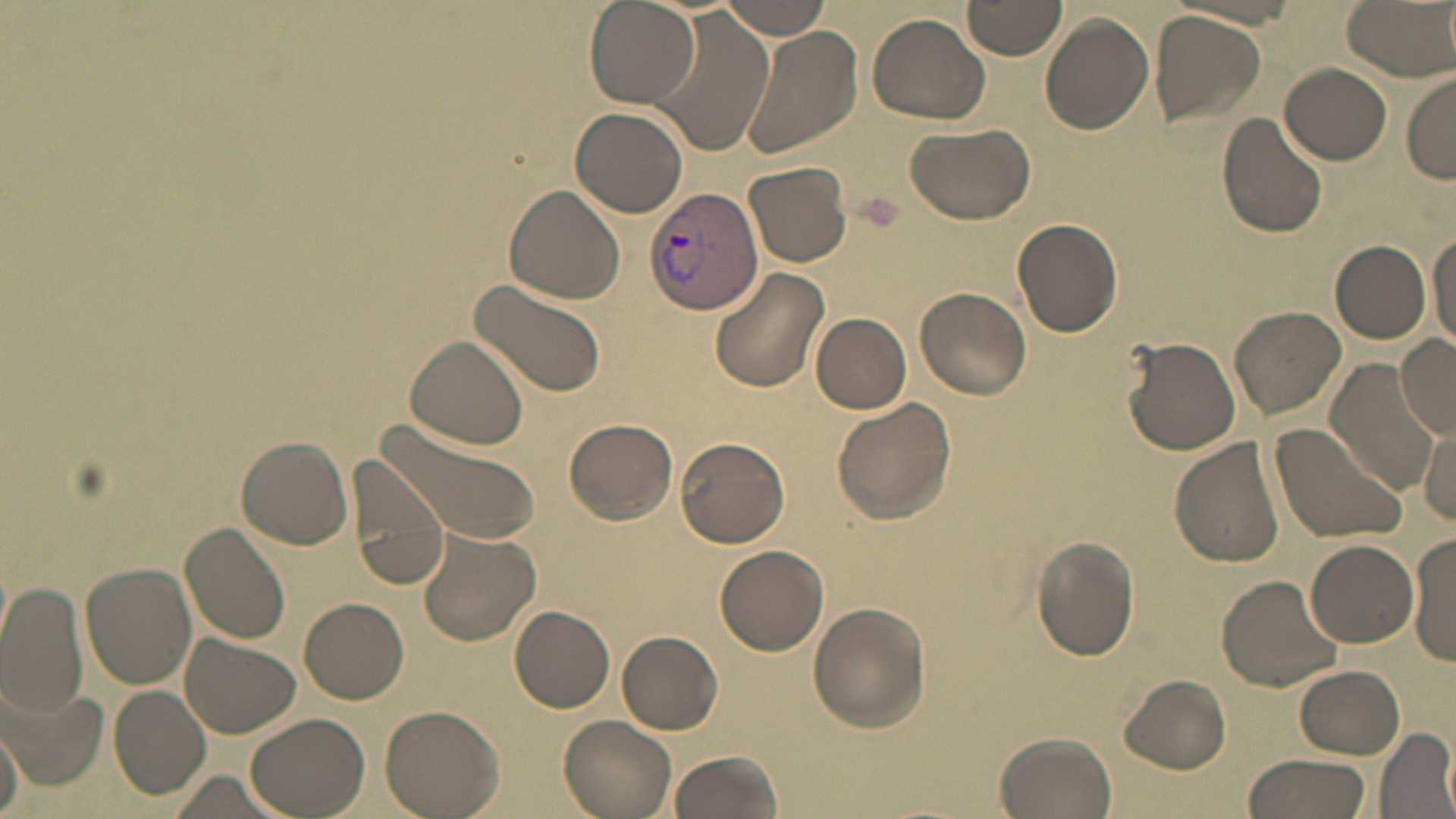

Summary:
  - Coordinate format: approximate bounding boxes as (x1,y1)-(x2,y2) corner pairs in pixels
  - Plasmodium vivax-infected red blood cell locations: (645,186)-(764,316)
  - Uninfected red blood cell locations: (717,0)-(835,38), (965,0)-(1066,59), (1339,0)-(1456,79), (586,2)-(699,107), (649,8)-(772,156), (1151,10)-(1267,128), (866,11)-(991,125), (1040,13)-(1155,135), (738,25)-(863,160), (1280,62)-(1392,165), (1403,74)-(1456,183), (569,107)-(688,218), (1217,110)-(1331,239), (906,120)-(1039,226), (742,161)-(851,267), (504,185)-(624,303), (1011,218)-(1124,337), (1429,229)-(1456,351), (1330,239)-(1431,344), (709,268)-(831,394), (468,279)-(605,397), (915,286)-(1032,399), (1229,305)-(1347,421), (811,313)-(912,412), (1395,332)-(1456,439), (404,335)-(531,450), (1121,336)-(1242,455), (1324,361)-(1443,496), (830,397)-(957,523), (377,415)-(541,548), (565,418)-(677,524), (1268,421)-(1407,546), (1419,423)-(1456,525), (234,435)-(353,550), (673,435)-(792,548), (1171,437)-(1287,569), (344,455)-(450,592), (182,522)-(291,644), (416,527)-(541,645), (1408,532)-(1456,667), (1030,534)-(1141,661), (1307,539)-(1417,647), (713,545)-(829,655), (80,563)-(195,688), (1215,574)-(1344,692), (0,580)-(88,718), (299,598)-(408,703), (808,601)-(932,732), (509,605)-(615,712), (618,631)-(722,733), (181,634)-(300,737), (1294,664)-(1403,758), (1119,674)-(1232,773), (2,678)-(101,788), (108,686)-(210,800), (380,704)-(504,819), (245,710)-(370,816), (558,713)-(677,818), (1,726)-(25,818), (1375,726)-(1456,818), (993,732)-(1119,819), (667,750)-(785,819), (1241,753)-(1372,819)
  - Slide-level diagnosis: Plasmodium vivax
  - Magnification: 1000x
  - Preparation: thin blood smear
  - Image size: 1456×819 pixels
  - Stain: May-Grünwald-Giemsa
  - Modality: optical microscopy
  - Field of view: one of a larger specimen